Classify this cell by malaria status.
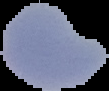
Parasitized.

preparation = thin blood smear
image size = 109×91 pixels
image type = segmented cell region on a black background